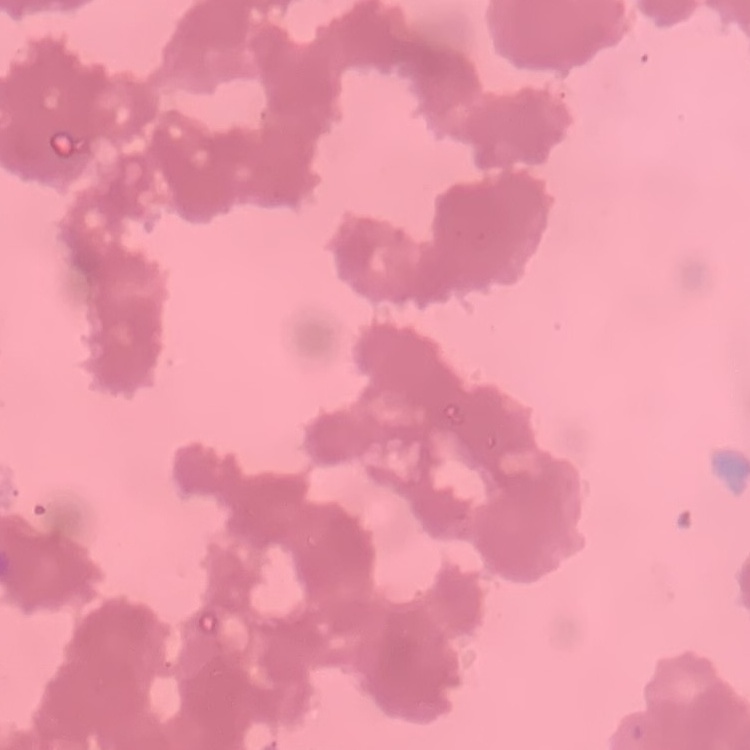

Summary:
  - Red blood cell morphology: rouleaux formation
  - Image type: one tile cut from a larger photomicrograph
  - Stain: Field's or Giemsa
  - Preparation: thin blood film